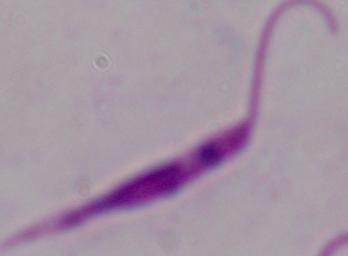
Photomicrograph. 1000x magnification. A Leishmania parasite is seen.